Point out each malaria parasite and each leukocyte.
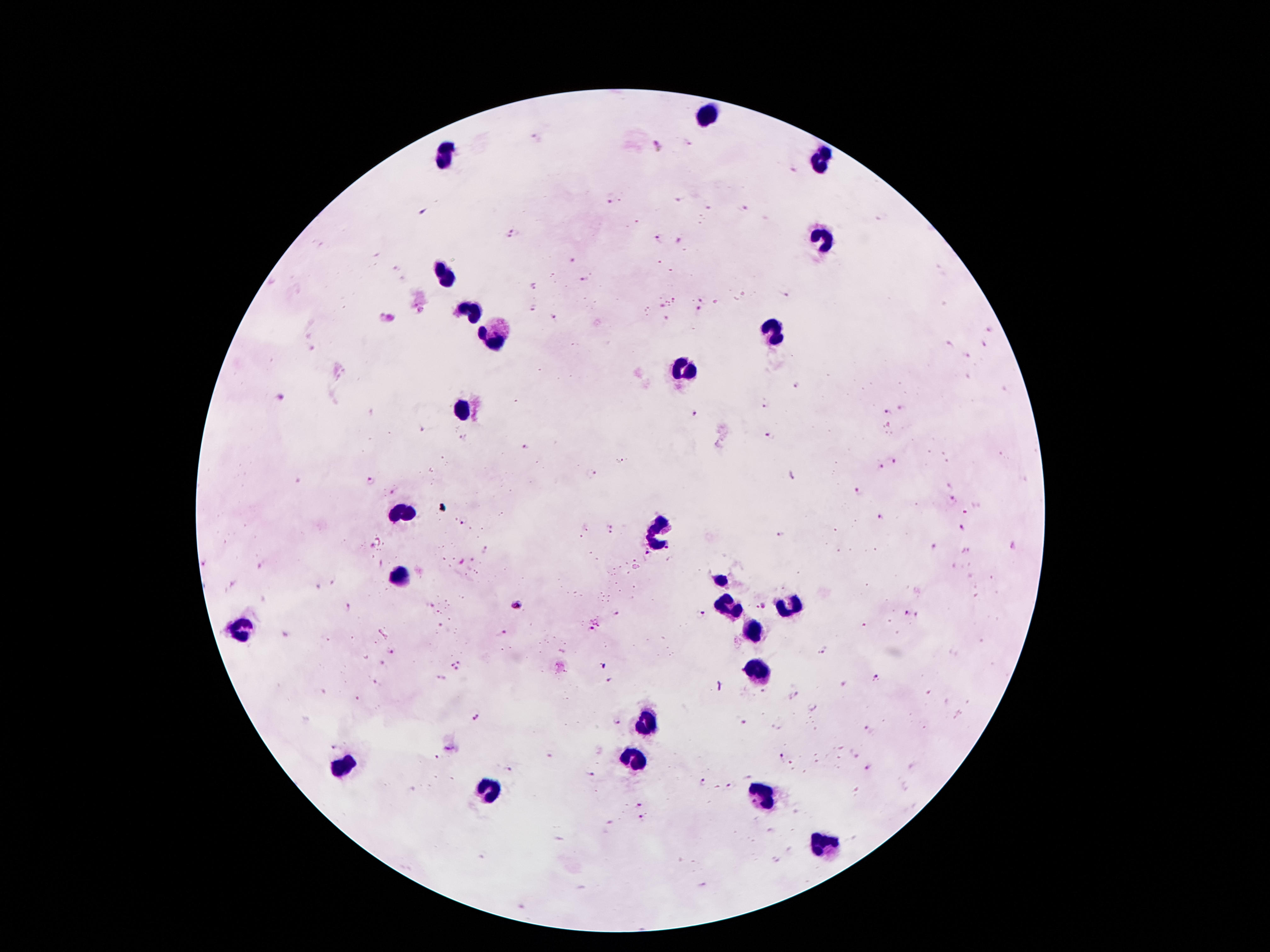
Approximate centers as [x, y] in pixels.
Malaria parasites: [535, 137], [687, 142], [658, 146], [791, 169], [610, 198], [680, 200], [710, 208], [744, 210], [423, 212], [881, 218], [514, 235], [658, 240], [680, 240], [573, 261], [395, 268], [403, 280], [584, 281], [532, 287], [784, 292], [701, 298], [661, 305], [531, 309], [698, 309], [422, 312], [391, 317], [555, 317], [380, 319], [665, 320], [990, 330], [983, 343], [949, 344], [968, 355], [796, 386], [278, 397], [769, 403], [901, 409], [888, 412], [693, 413], [423, 430], [768, 436], [525, 449], [892, 461], [880, 466], [592, 473], [790, 476], [370, 482], [855, 492], [393, 493], [950, 497], [966, 508], [879, 515], [464, 521], [963, 528], [610, 529], [780, 536], [1013, 546], [934, 547], [487, 550], [203, 561], [260, 566], [334, 580], [318, 586], [517, 604], [764, 605], [756, 606], [347, 607], [904, 612], [699, 614], [918, 614], [617, 616], [598, 623], [590, 631], [503, 632], [823, 649], [392, 651], [382, 662], [457, 664], [604, 666], [876, 677], [442, 679], [610, 681], [375, 682], [796, 696], [359, 698], [475, 716], [741, 720], [618, 721], [867, 727], [333, 748], [551, 754], [856, 756], [437, 757], [781, 757], [508, 769], [870, 770], [592, 775], [703, 783], [730, 786], [639, 803], [641, 818].
Leukocytes: [706, 112], [447, 153], [820, 162], [823, 241], [445, 273], [470, 311], [493, 334], [772, 334], [684, 370], [462, 409], [403, 513], [658, 528], [399, 578], [725, 580], [788, 603], [729, 605], [239, 631], [752, 633], [753, 667], [646, 723], [633, 755], [342, 765], [488, 787], [761, 791], [827, 843].

Single field of view. Photographed through the microscope eyepiece with a smartphone camera. Thick blood film. 100x magnification. Patient malaria status: infected with Plasmodium falciparum. Giemsa stain. Image is 1270×952 pixels.